Give the preparation type.
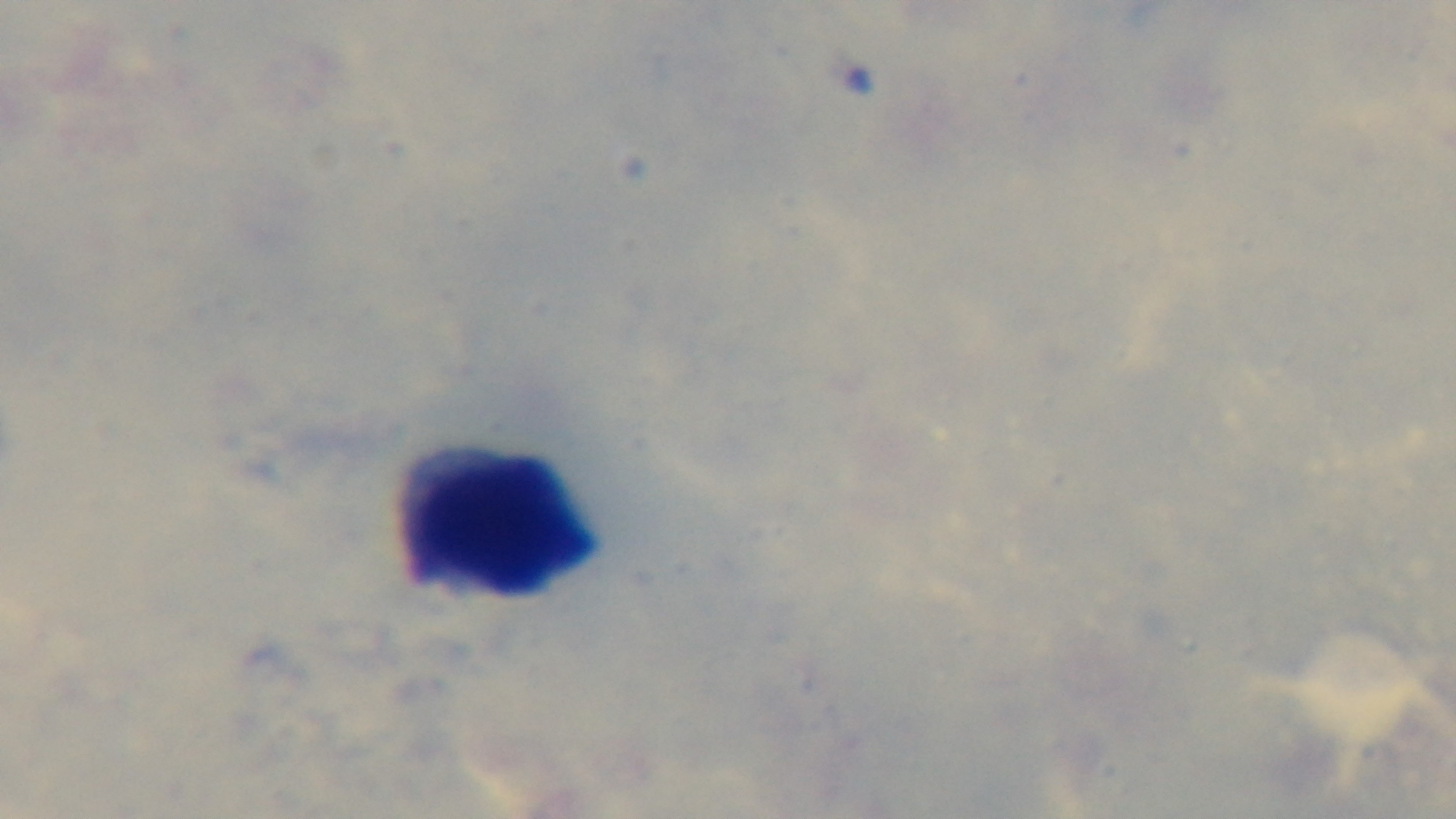

Thick.

{
  "malaria_status": "negative",
  "field_of_view": "one from the slide",
  "objective": "100x oil immersion",
  "capture": "mounted 4K digital camera",
  "modality": "light microscopy",
  "stain": "Giemsa"
}